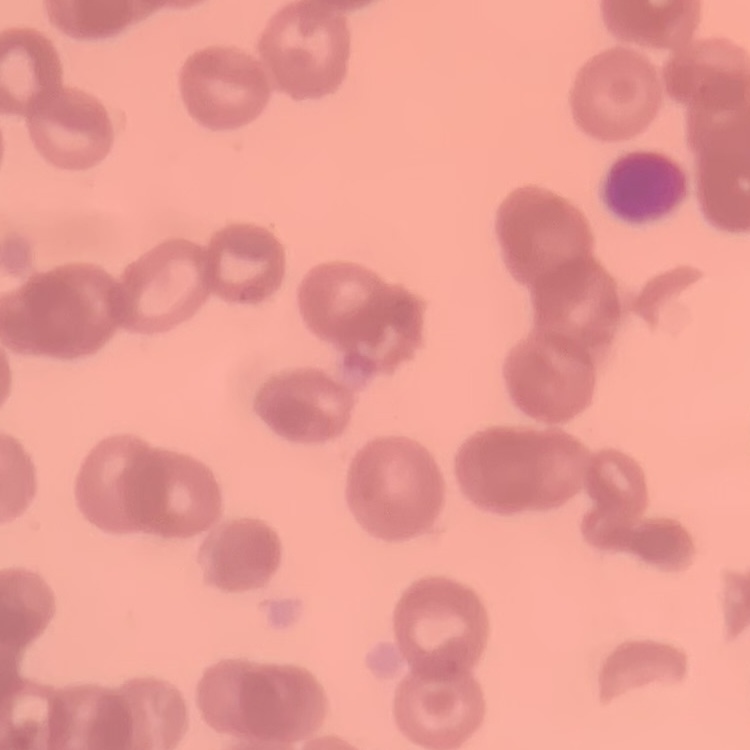
The red blood cells exhibit rouleaux formation. Thin blood film. One tile cut from a larger photomicrograph. Field's or Giemsa stain.